Identify the parasite.
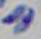
This is Toxoplasma gondii.

1000x magnification. Photomicrograph.